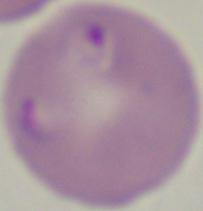

1000x magnification. Photomicrograph. A Babesia parasite is seen.